Classify this cell by malaria status.
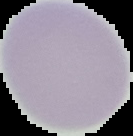
It is uninfected.

image_type: segmented cell region on a black background
preparation: thin blood smear
image_size: 133×136 pixels